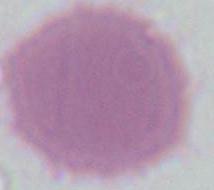

An erythrocyte is seen. Micrograph. Captured at 1000x magnification.